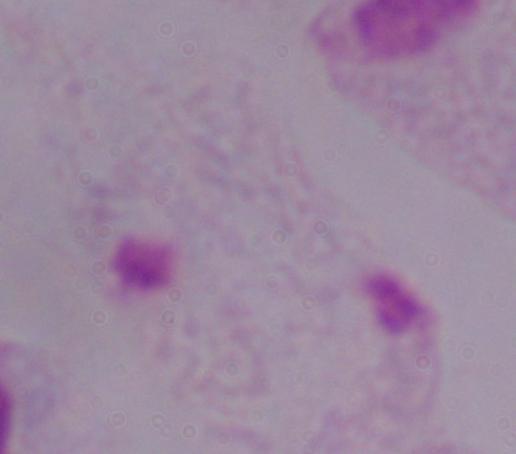
Summary:
  - Identification: trichomonad
  - Magnification: 1000x
  - Modality: micrograph